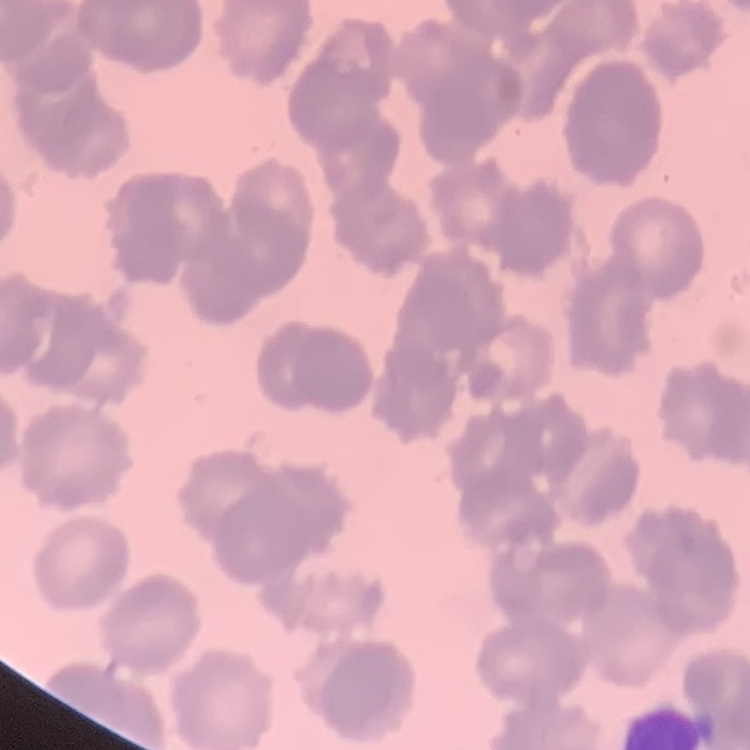

The erythrocytes exhibit rouleaux formation. One tile cut from a larger photomicrograph. Stained with either Field's or Giemsa. Thin blood smear.